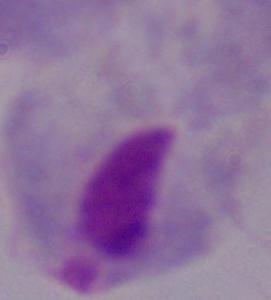

Summary:
  - Identification: trichomonad
  - Magnification: 1000x
  - Modality: photomicrograph